State which parasite is depicted.
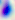
This is Toxoplasma gondii.

Summary:
  - Modality: micrograph
  - Magnification: 400x